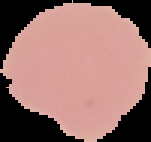

Malaria status: uninfected. Image is 151×142 pixels. From a thin blood smear. Segmented cell region on a black background.